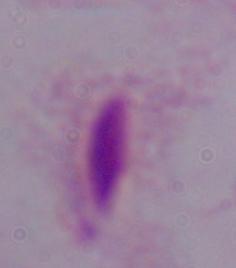
identification = trichomonad
magnification = 1000x
modality = micrograph